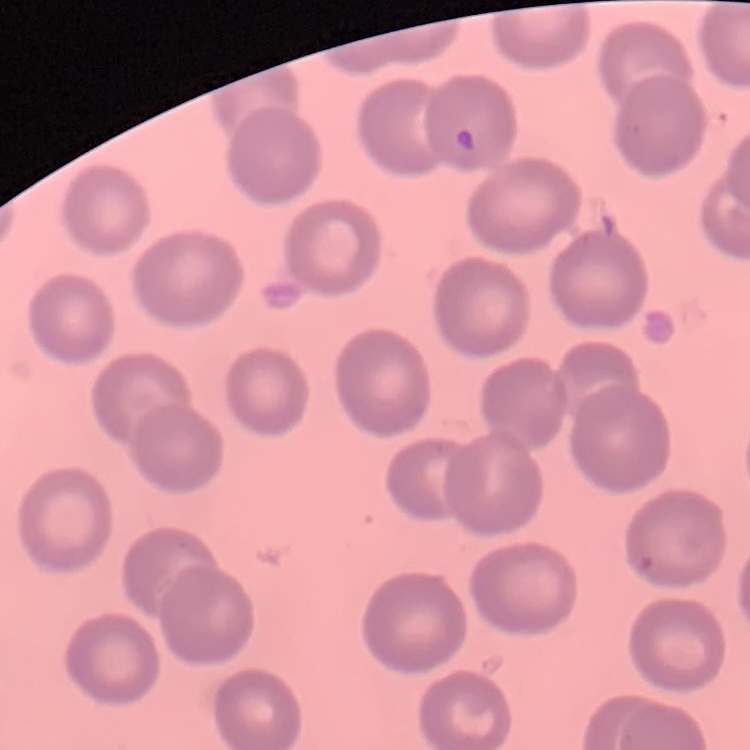 The red blood cells exhibit no rouleaux formation. Square crop of a larger photomicrograph. Thin peripheral smear. Field's or Giemsa stain.